Give the position of every Plasmodium falciparum parasite, noting its life-cycle stage.
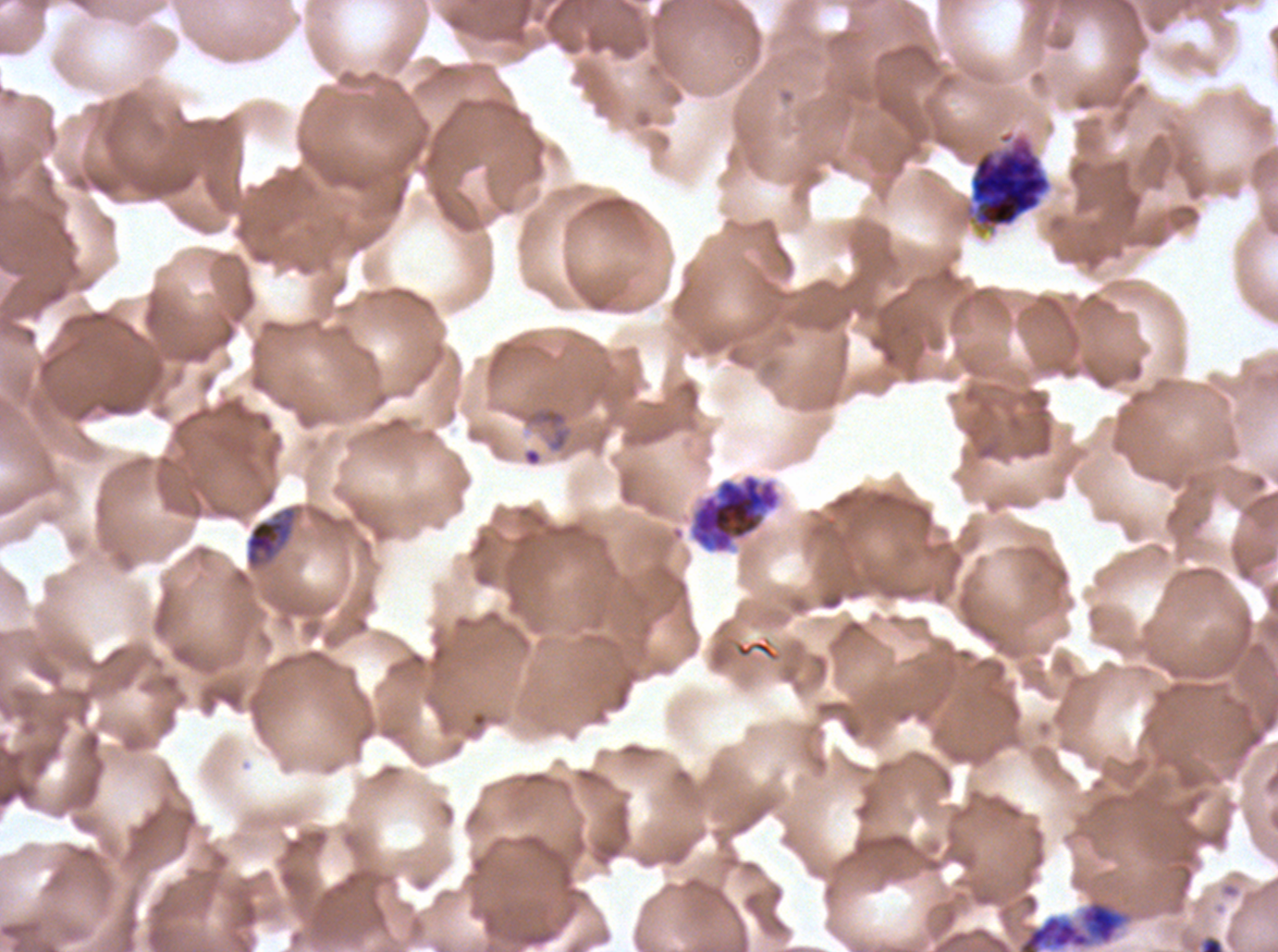
Approximate bounding boxes as [x1, y1, x2, y2] in pixels.
Rings: [528, 407, 570, 452].
Late trophozoites: [245, 507, 296, 568].
Early schizonts: [963, 129, 1052, 234].
Late schizonts: [690, 473, 780, 554], [1017, 899, 1126, 951].
No late-ring/early-trophozoite forms, mid trophozoites, segmenters, or gametocytes observed.

stain = Giemsa
specimen = ex-vivo Plasmodium falciparum culture from a patient in The Gambia, grown for 24 to 48 hours
life-cycle stages observed = ring, late trophozoite, early schizont, late schizont
preparation = thin blood smear
field of view = one sub-image of a larger composite
image size = 1278×952 pixels